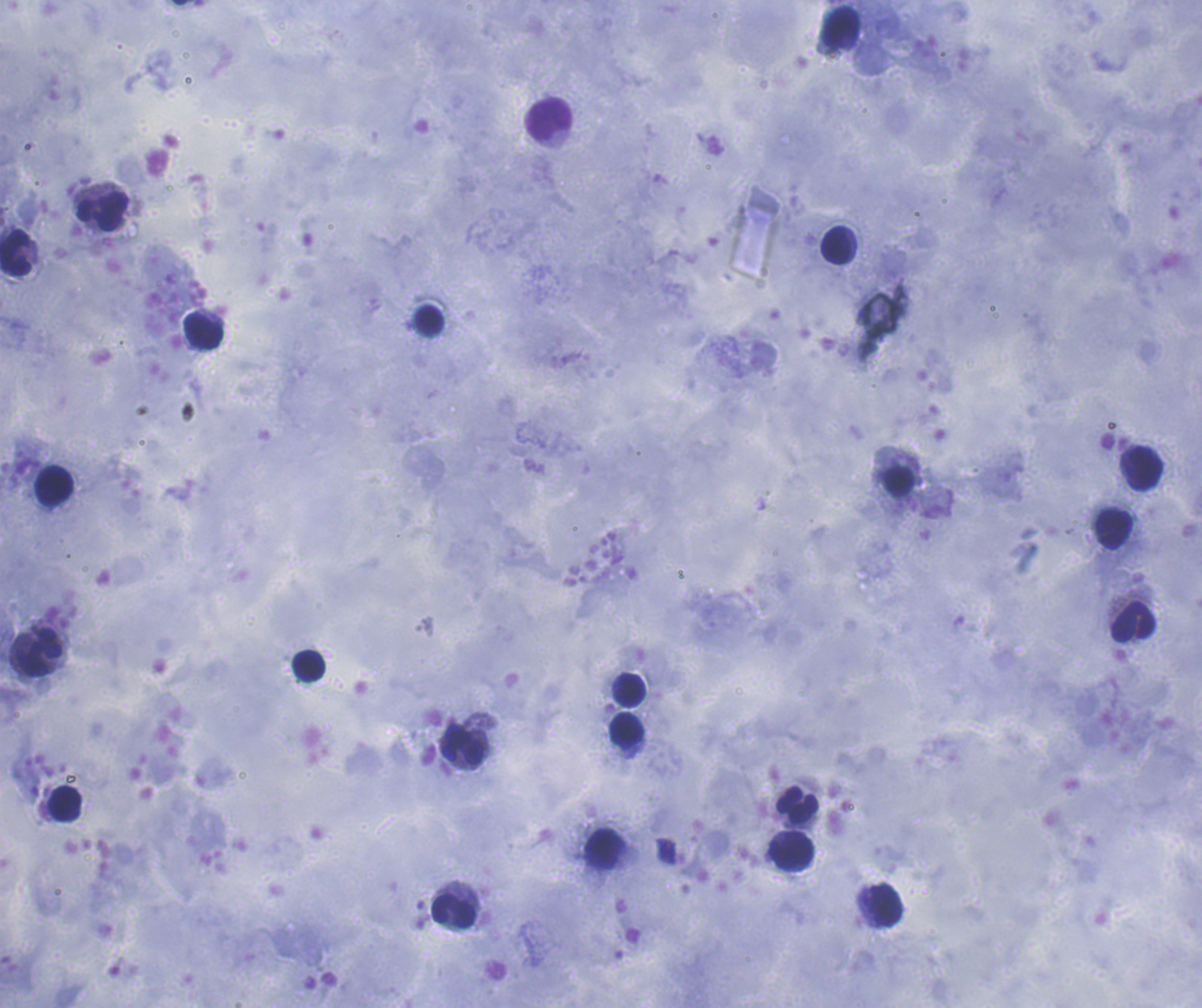

Approximate centers as (x, y) in pixels. Leukocyte locations: (841, 27), (549, 119), (102, 211), (837, 245), (15, 252), (429, 320), (203, 331), (1145, 468), (898, 482), (53, 485), (1114, 528), (1134, 621), (40, 652), (308, 666), (631, 690), (626, 730), (462, 743), (64, 803), (797, 804), (604, 849), (792, 853), (888, 903), (454, 910). Single field of view. Romanowsky-stained preparation. Previously used in an actual diagnosis. Coloration quality: good. Image is 1202×1008 pixels. Captured at 100x magnification. Result: no Plasmodium parasites seen. Background quality: satisfactory. Thick blood smear.